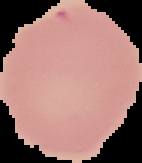
result = no Plasmodium parasites detected
preparation = thin blood film
image type = cell region segmented out of the field of view; surrounding area masked to black
image size = 142×163 pixels